State which parasite is depicted.
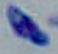
Toxoplasma gondii.

Summary:
  - Magnification: 1000x
  - Modality: photomicrograph